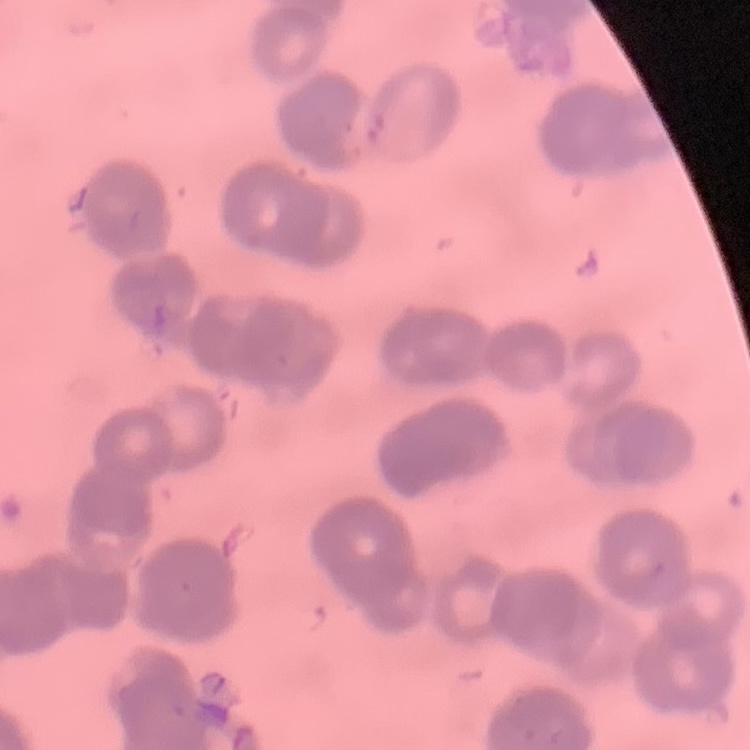
Summary:
  - Red blood cell morphology: rouleaux formation
  - Stain: Field's or Giemsa
  - Image type: one tile cut from a larger photomicrograph
  - Preparation: thin peripheral smear